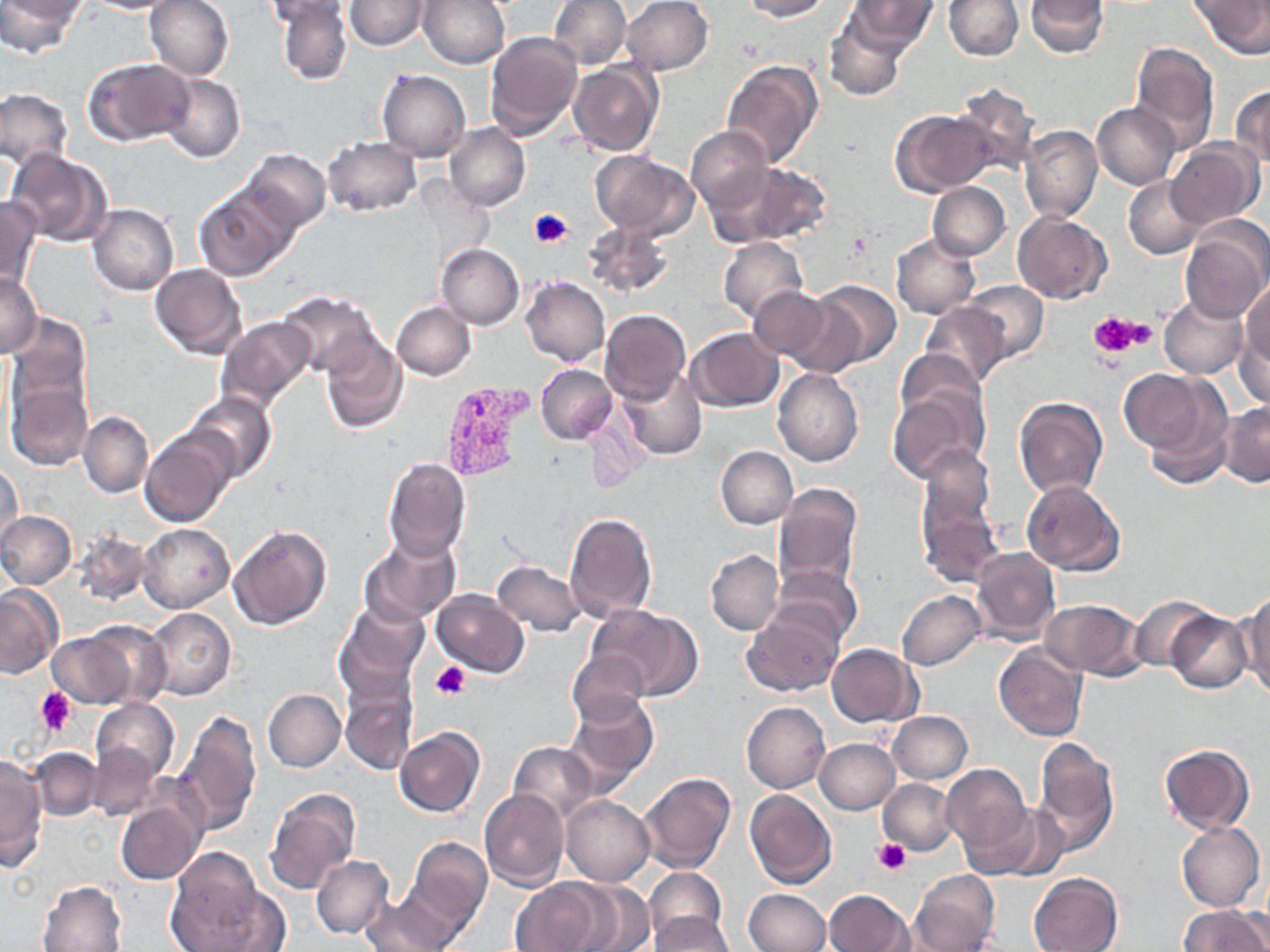
Summary:
  - Coordinate format: approximate bounding boxes as (x1, y1, x2, y2) in pixels
  - Plasmodium vivax-infected red blood cell locations: (438, 381, 536, 484)
  - Uninfected red blood cell locations: (0, 0, 79, 58), (82, 0, 183, 14), (145, 0, 234, 80), (276, 0, 352, 85), (344, 0, 428, 50), (418, 0, 510, 70), (551, 0, 631, 70), (622, 0, 714, 75), (741, 0, 830, 20), (847, 0, 937, 53), (943, 0, 1022, 61), (1027, 0, 1109, 57), (1191, 0, 1270, 57), (261, 1, 354, 28), (824, 16, 906, 103), (485, 30, 582, 138), (1129, 43, 1221, 153), (85, 58, 194, 147), (720, 61, 823, 168), (568, 62, 661, 155), (377, 70, 470, 161), (159, 73, 244, 164), (951, 82, 1040, 175), (1231, 85, 1269, 168), (1, 88, 73, 167), (1092, 102, 1180, 190), (892, 109, 997, 195), (444, 123, 530, 211), (1019, 124, 1102, 223), (686, 126, 770, 214), (323, 135, 421, 217), (1166, 139, 1262, 230), (6, 148, 114, 246), (241, 149, 330, 233), (590, 150, 699, 238), (713, 159, 832, 247), (1123, 176, 1207, 260), (928, 182, 1010, 259), (194, 186, 294, 280), (0, 196, 42, 286), (88, 204, 178, 296), (1012, 212, 1111, 304), (1179, 218, 1270, 321), (582, 220, 675, 299), (891, 234, 980, 319), (719, 238, 808, 322), (437, 243, 524, 330), (150, 264, 247, 360), (1, 271, 42, 358), (521, 278, 610, 367), (1241, 278, 1270, 370), (801, 281, 901, 371), (964, 281, 1049, 364), (749, 286, 833, 361), (279, 291, 379, 377), (1158, 294, 1249, 378), (392, 302, 475, 380), (918, 302, 1015, 388), (600, 309, 690, 403), (217, 316, 317, 412), (5, 317, 91, 437), (1236, 319, 1269, 411), (688, 328, 783, 410), (320, 333, 408, 434), (536, 364, 617, 445), (1126, 366, 1239, 482), (618, 369, 708, 460), (773, 369, 864, 467), (8, 377, 91, 470), (888, 383, 991, 483), (186, 392, 275, 481), (1013, 398, 1109, 500), (1217, 402, 1270, 486), (79, 411, 154, 497), (142, 431, 236, 527), (919, 445, 996, 535), (716, 446, 797, 528), (383, 457, 471, 561), (1, 458, 23, 547), (1021, 480, 1126, 577), (771, 485, 863, 593), (916, 495, 1004, 590), (563, 510, 658, 623), (0, 511, 76, 590), (0, 519, 148, 595), (137, 522, 235, 612), (228, 523, 332, 630), (74, 532, 153, 607), (359, 534, 460, 626), (970, 547, 1060, 646), (705, 549, 783, 636), (490, 560, 585, 637), (773, 564, 861, 645), (0, 584, 65, 680), (432, 589, 529, 676), (897, 590, 987, 671), (1238, 592, 1270, 696), (1131, 595, 1213, 671), (1040, 598, 1143, 678), (336, 601, 428, 695), (589, 606, 700, 700), (743, 606, 842, 697), (146, 607, 235, 701), (1166, 611, 1251, 693), (47, 627, 143, 709), (994, 643, 1088, 741), (828, 644, 921, 726), (567, 651, 649, 726), (341, 685, 416, 775), (263, 688, 345, 772), (566, 693, 658, 790), (90, 697, 179, 785), (742, 701, 830, 794), (175, 709, 263, 836), (887, 711, 972, 783), (395, 726, 485, 818), (815, 738, 899, 814), (1031, 738, 1120, 854), (508, 741, 597, 823), (88, 742, 163, 820), (1159, 745, 1254, 834), (30, 748, 102, 819), (0, 754, 48, 870), (941, 764, 1031, 856), (639, 773, 736, 875), (879, 778, 958, 856), (264, 787, 360, 895), (745, 788, 837, 889), (479, 789, 569, 891), (562, 794, 655, 885), (115, 797, 203, 884), (979, 803, 1068, 883), (1176, 822, 1264, 911), (405, 838, 492, 933), (165, 849, 278, 952), (311, 854, 395, 940), (643, 867, 727, 948), (909, 870, 999, 951), (1028, 872, 1122, 952), (511, 878, 613, 952), (38, 880, 128, 952), (557, 883, 654, 952), (743, 889, 830, 952), (824, 889, 911, 952), (360, 897, 455, 951), (1178, 905, 1270, 952), (648, 913, 737, 952)
  - Platelet locations: (528, 209, 573, 248), (847, 229, 873, 254), (1087, 311, 1146, 359), (431, 661, 470, 700), (35, 688, 76, 735), (873, 838, 910, 877)
  - Slide-level diagnosis: Plasmodium vivax
  - Magnification: 1000x
  - Field of view: one of a larger specimen
  - Modality: optical microscopy
  - Preparation: thin blood smear
  - Image size: 1270×952 pixels
  - Stain: May-Grünwald-Giemsa